State the preparation type.
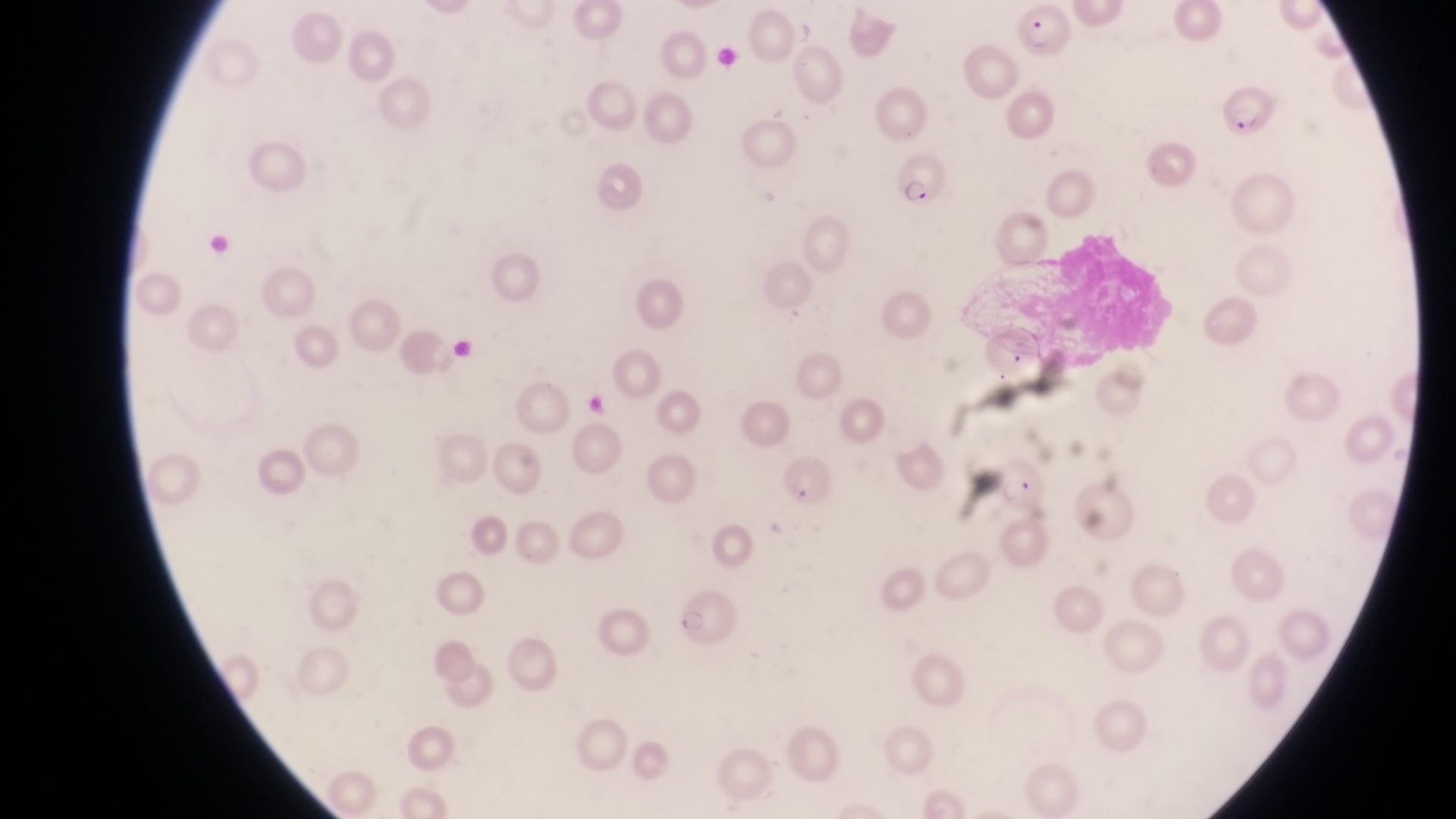

This is a thin smear.

{
  "field_of_view": "single",
  "image_size": "1456×819 pixels",
  "magnification": "1000x",
  "country": "Uganda",
  "capture": "smartphone photograph through the eyepiece of an Olympus CX-23 microscope",
  "parasitised_red_blood_cell_locations": "approximate bounding boxes as {left, top, right, bottom} in pixels: {1018, 5, 1070, 59}, {1215, 85, 1281, 143}, {885, 158, 943, 207}, {986, 447, 1047, 510}, {782, 457, 838, 510}, {668, 592, 740, 647}"
}